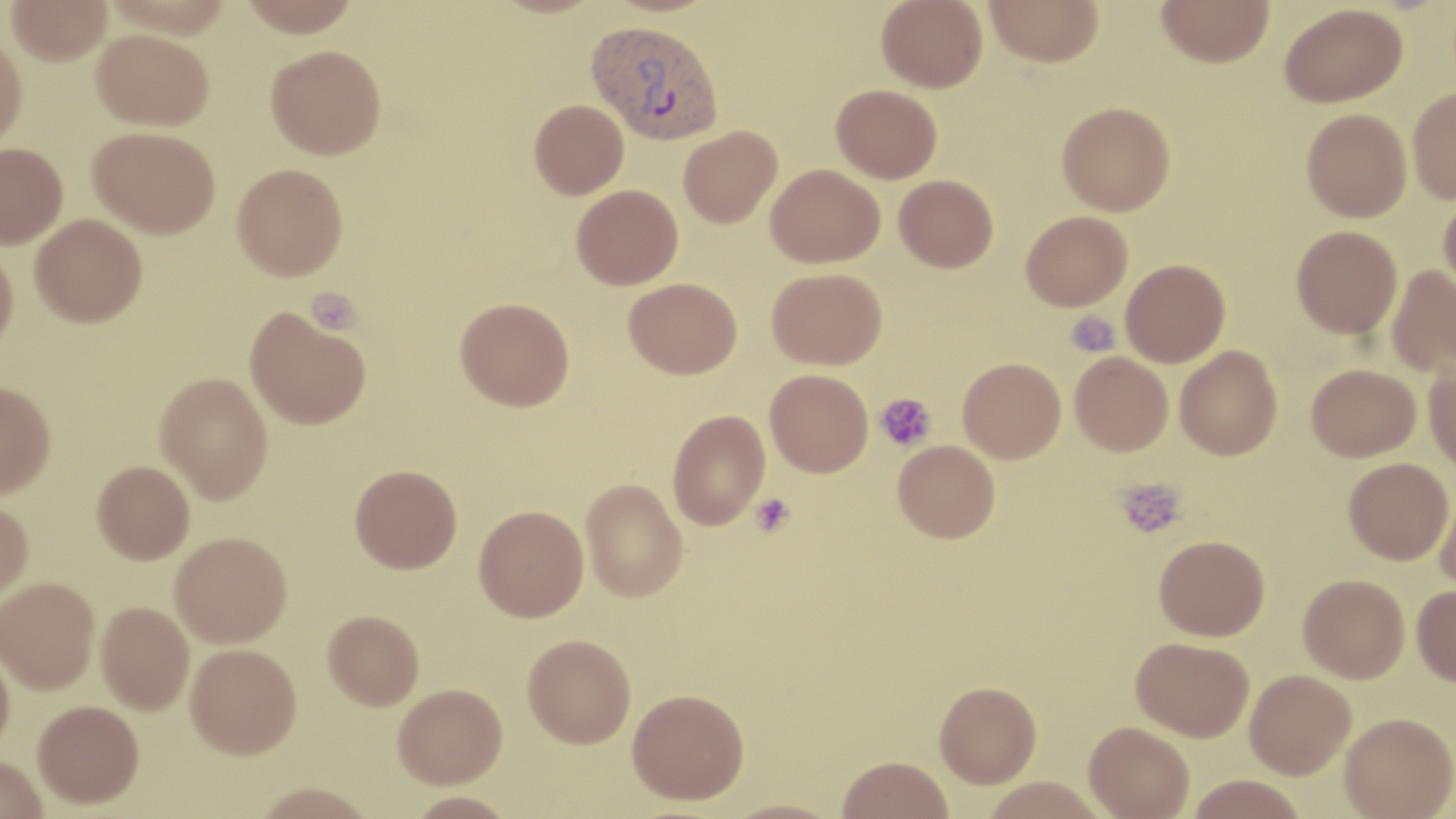

slide-level diagnosis = Plasmodium vivax
image size = 1456×819 pixels
Plasmodium vivax-infected red blood cell locations = approximate bounding boxes as named x1/y1/x2/y2 corners in pixels: (x1=587, y1=20, x2=725, y2=145)
modality = optical microscopy
uninfected red blood cell locations = approximate bounding boxes as named x1/y1/x2/y2 corners in pixels: (x1=5, y1=0, x2=112, y2=65), (x1=237, y1=0, x2=363, y2=36), (x1=877, y1=0, x2=988, y2=92), (x1=984, y1=0, x2=1104, y2=67), (x1=1156, y1=0, x2=1274, y2=67), (x1=1279, y1=3, x2=1407, y2=107), (x1=92, y1=28, x2=213, y2=130), (x1=0, y1=33, x2=27, y2=152), (x1=265, y1=44, x2=387, y2=159), (x1=831, y1=84, x2=942, y2=183), (x1=1407, y1=87, x2=1456, y2=204), (x1=529, y1=98, x2=629, y2=199), (x1=1057, y1=101, x2=1175, y2=216), (x1=1302, y1=108, x2=1412, y2=222), (x1=88, y1=126, x2=220, y2=238), (x1=678, y1=126, x2=782, y2=227), (x1=0, y1=143, x2=67, y2=249), (x1=232, y1=163, x2=348, y2=280), (x1=766, y1=163, x2=885, y2=267), (x1=894, y1=174, x2=998, y2=272), (x1=571, y1=184, x2=683, y2=289), (x1=1438, y1=193, x2=1456, y2=299), (x1=1021, y1=210, x2=1133, y2=311), (x1=30, y1=214, x2=147, y2=326), (x1=1291, y1=225, x2=1402, y2=338), (x1=0, y1=243, x2=18, y2=356), (x1=1121, y1=259, x2=1230, y2=367), (x1=1386, y1=265, x2=1456, y2=377), (x1=767, y1=267, x2=887, y2=369), (x1=624, y1=277, x2=742, y2=378), (x1=455, y1=297, x2=575, y2=410), (x1=244, y1=307, x2=371, y2=429), (x1=1175, y1=345, x2=1283, y2=460), (x1=1069, y1=352, x2=1173, y2=456), (x1=957, y1=357, x2=1066, y2=463), (x1=1423, y1=360, x2=1456, y2=474), (x1=1306, y1=363, x2=1421, y2=461), (x1=765, y1=369, x2=873, y2=477), (x1=154, y1=372, x2=274, y2=503), (x1=0, y1=380, x2=56, y2=498), (x1=667, y1=409, x2=770, y2=530), (x1=893, y1=440, x2=1000, y2=542), (x1=1344, y1=457, x2=1453, y2=564), (x1=92, y1=460, x2=194, y2=563), (x1=350, y1=464, x2=462, y2=573), (x1=581, y1=478, x2=688, y2=602), (x1=1435, y1=488, x2=1456, y2=596), (x1=0, y1=499, x2=33, y2=603), (x1=474, y1=504, x2=589, y2=621), (x1=170, y1=531, x2=292, y2=647), (x1=1154, y1=535, x2=1270, y2=640), (x1=1298, y1=574, x2=1410, y2=683), (x1=0, y1=577, x2=100, y2=693), (x1=1412, y1=585, x2=1456, y2=686), (x1=96, y1=600, x2=194, y2=714), (x1=323, y1=609, x2=424, y2=709), (x1=523, y1=633, x2=636, y2=747), (x1=1132, y1=637, x2=1255, y2=741), (x1=0, y1=643, x2=15, y2=756), (x1=185, y1=643, x2=302, y2=758), (x1=1245, y1=669, x2=1356, y2=779), (x1=934, y1=681, x2=1042, y2=787), (x1=393, y1=683, x2=507, y2=787), (x1=627, y1=688, x2=750, y2=804), (x1=33, y1=700, x2=144, y2=808), (x1=1340, y1=712, x2=1455, y2=818), (x1=1084, y1=720, x2=1194, y2=819), (x1=837, y1=755, x2=954, y2=819), (x1=0, y1=757, x2=48, y2=819), (x1=1185, y1=775, x2=1309, y2=818), (x1=980, y1=777, x2=1109, y2=819), (x1=252, y1=782, x2=377, y2=819), (x1=722, y1=799, x2=844, y2=819)
stain = May-Grünwald-Giemsa
magnification = 1000x
platelet locations = approximate bounding boxes as named x1/y1/x2/y2 corners in pixels: (x1=307, y1=287, x2=361, y2=335), (x1=1065, y1=311, x2=1120, y2=358), (x1=875, y1=392, x2=937, y2=452), (x1=1116, y1=477, x2=1187, y2=539), (x1=750, y1=493, x2=795, y2=537)
field of view = single
preparation = thin blood film